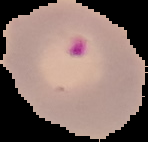 From a thin blood film. Image is 148×142 pixels. Segmented cell region on a black background. Result: malaria parasites identified.